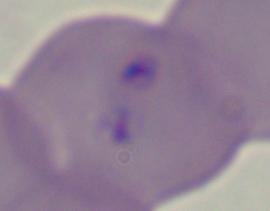
Summary:
  - Modality: photomicrograph
  - Magnification: 1000x
  - Identification: Babesia